Comment on the morphology of the erythrocytes.
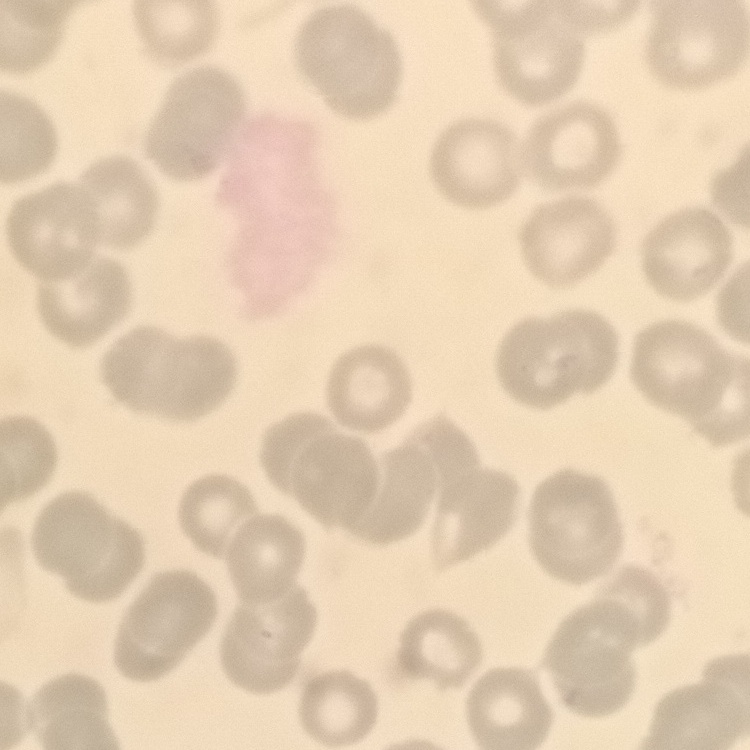
No rouleaux formation.

Summary:
  - Stain: Field's or Giemsa
  - Preparation: thin blood smear
  - Image type: one tile cut from a larger photomicrograph